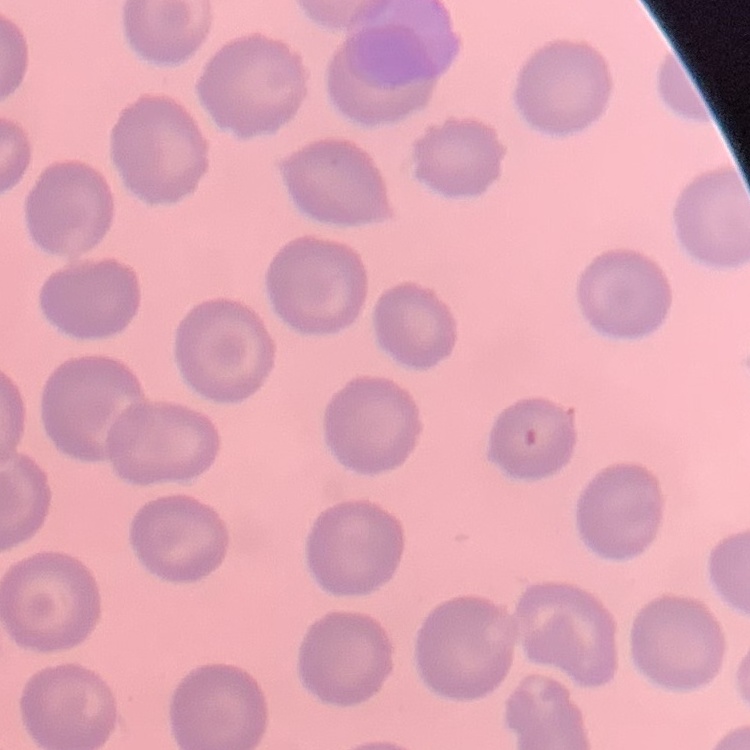
erythrocyte_morphology: no rouleaux formation
stain: Field's or Giemsa
preparation: thin blood film
image_type: square crop of a larger photomicrograph